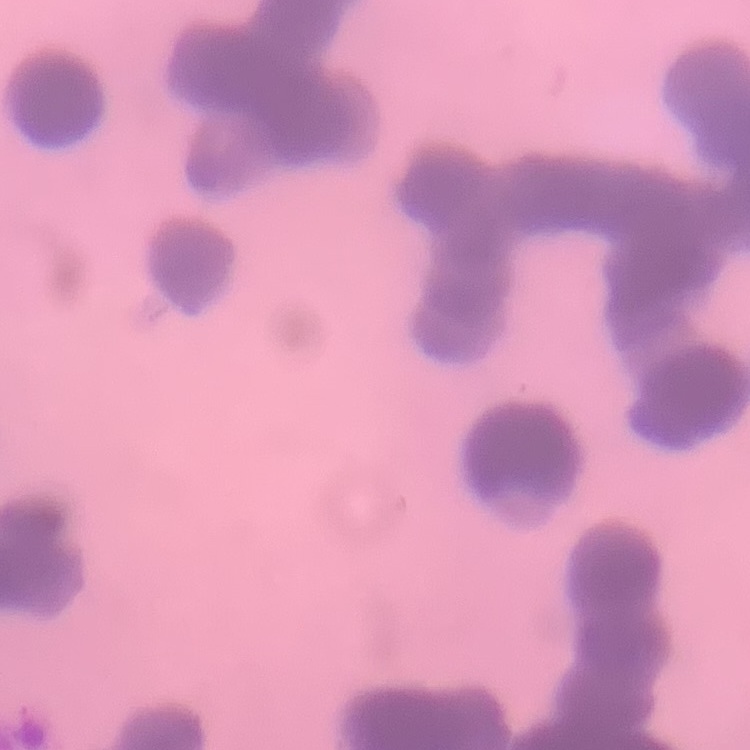

Summary:
  - Red blood cell morphology: rouleaux formation
  - Stain: Field's or Giemsa
  - Image type: square crop of a larger photomicrograph
  - Preparation: thin blood film